Classify this cell by malaria status.
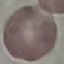

Uninfected.

image_type: automatically extracted cell patch, resized to 64 × 64 pixels
capture: smartphone camera at the microscope eyepiece
preparation: thin blood smear
stain: Giemsa